Classify this cell by malaria status.
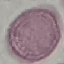

Uninfected.

Automatically extracted cell patch, resized to 64 × 64 pixels. Acquired by smartphone through the microscope eyepiece. Thin blood smear. Giemsa stain.